Report the malaria status of this cell.
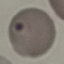
It is uninfected.

Summary:
  - Stain: Giemsa
  - Image type: automatically extracted cell patch, resized to 64 × 64 pixels
  - Preparation: thin blood film
  - Capture: smartphone camera at the microscope eyepiece